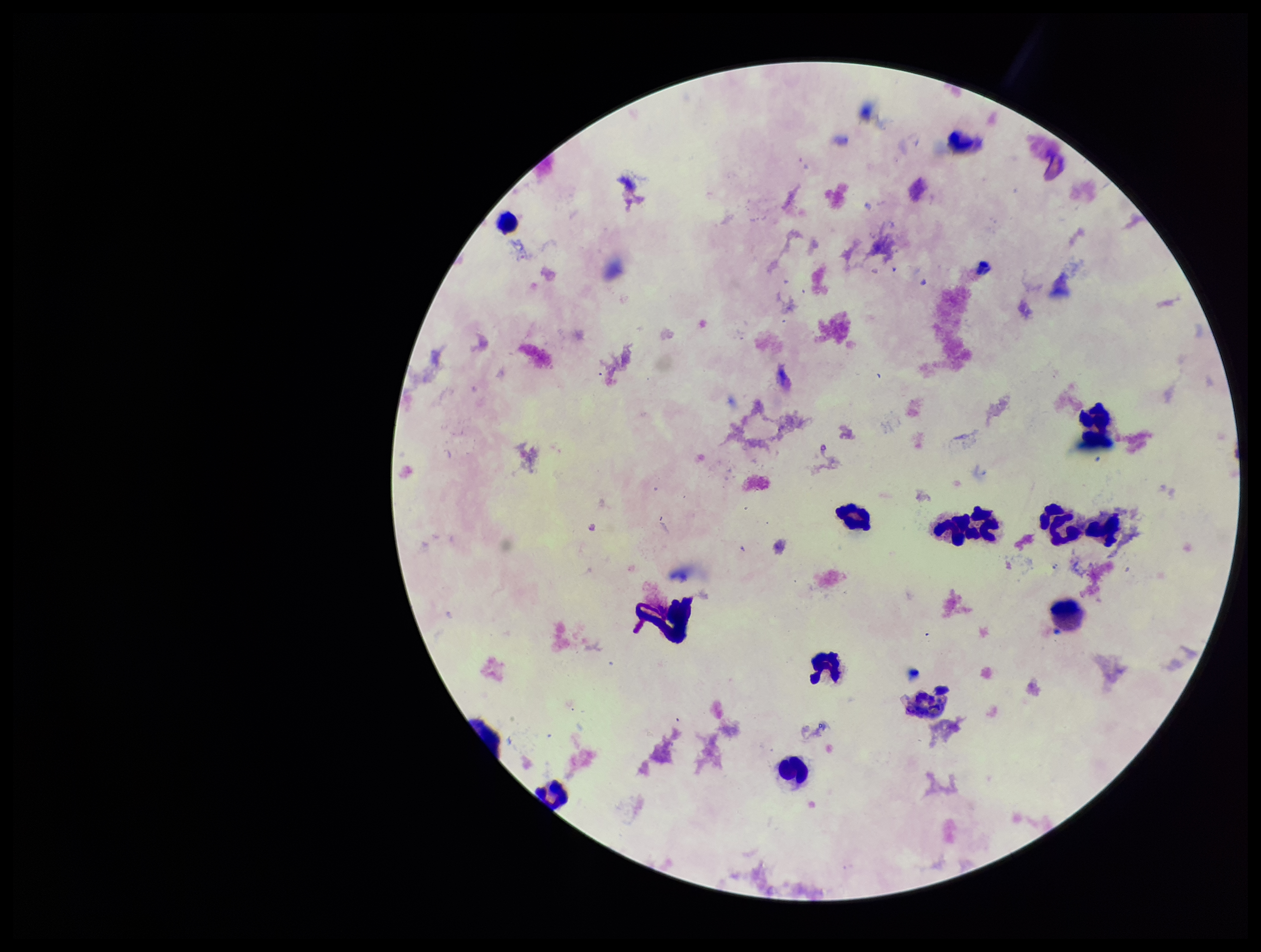
capture = smartphone photograph through the microscope eyepiece
patient malaria status = negative
field of view = single
parasite count = 0
image size = 1261×952 pixels
stain = Giemsa
leukocyte count = 12
Plasmodium parasites = none detected
preparation = thick blood smear